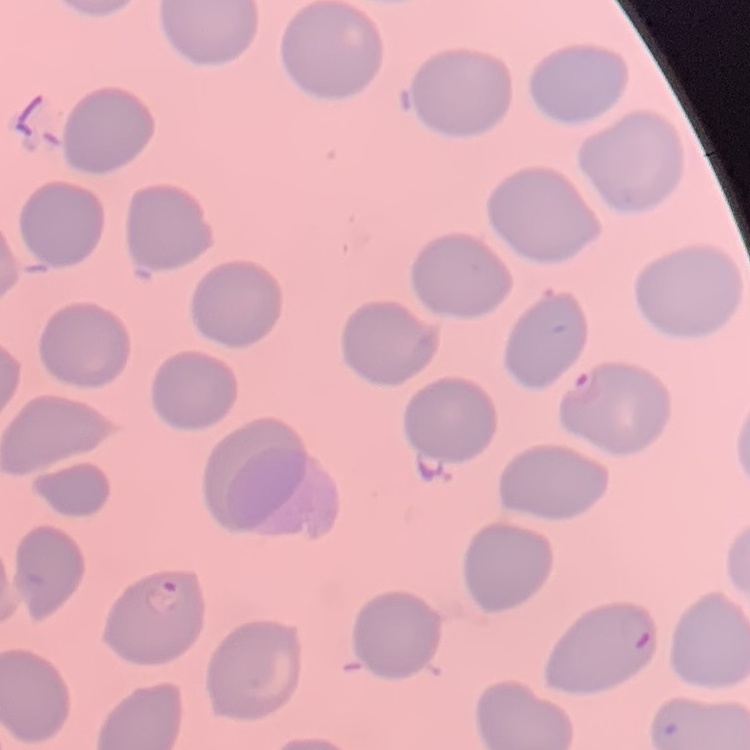

The red blood cells show no rouleaux formation. Thin peripheral smear. Stained with either Field's or Giemsa. One tile cut from a larger photomicrograph.